Assess this cell for malaria.
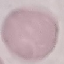

Uninfected.

Cell patch, automatically extracted from a larger field of view and resized to 64 × 64 pixels. Acquired by smartphone through the microscope eyepiece. Thin blood smear. Giemsa-stained preparation.